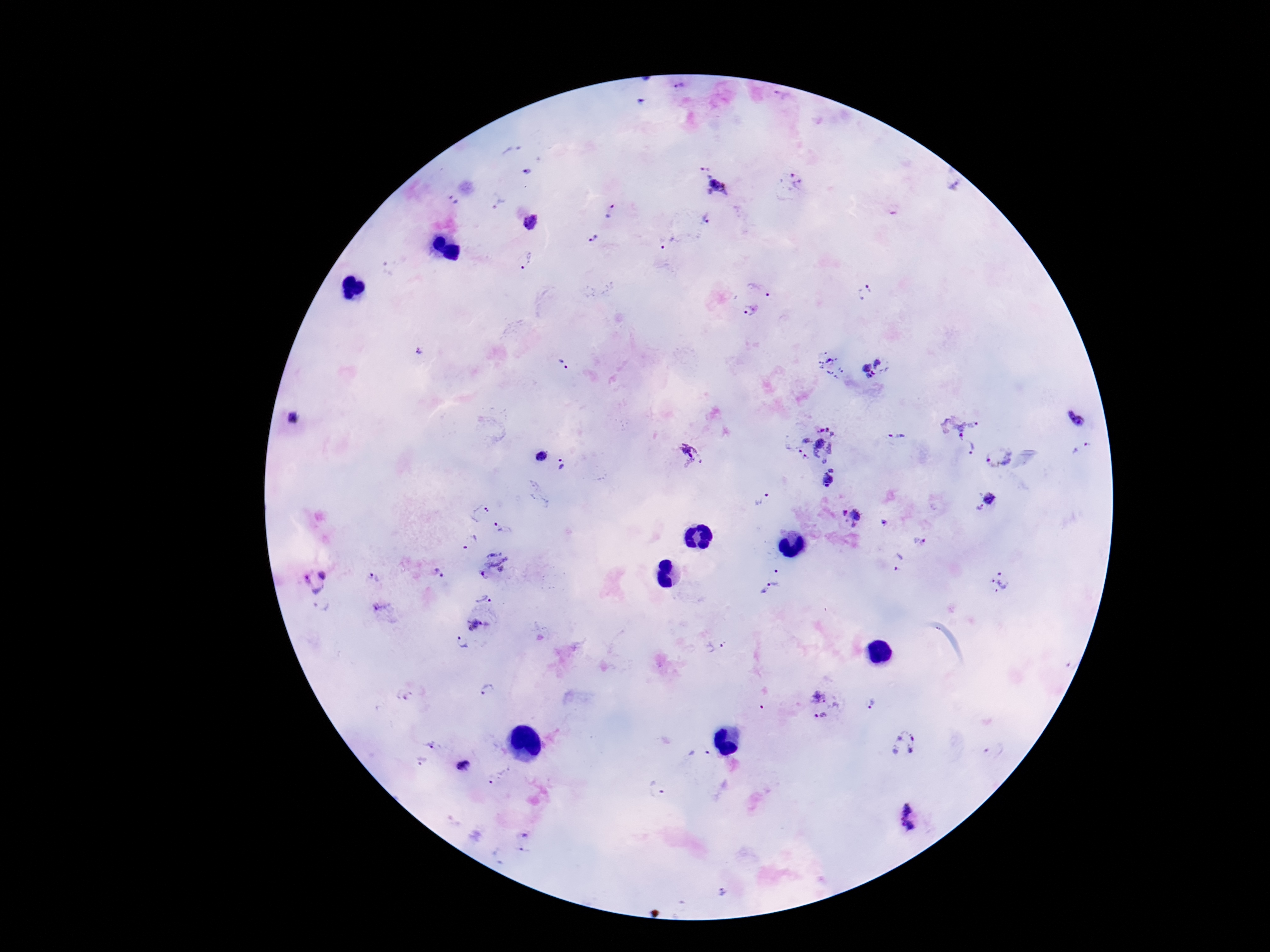

Approximate centers as (x, y) in pixels. Plasmodium parasite locations: (679, 84), (783, 99), (705, 164), (526, 173), (792, 181), (950, 184), (717, 185), (452, 200), (498, 204), (611, 210), (707, 216), (530, 222), (591, 239), (666, 243), (525, 262), (763, 286), (865, 291), (749, 309), (421, 348), (831, 363), (881, 364), (565, 366), (295, 416), (1077, 422), (957, 424), (898, 436), (811, 442), (970, 449), (1084, 452), (690, 454), (539, 455), (998, 456), (563, 467), (832, 468), (827, 481), (990, 496), (760, 500), (976, 509), (478, 512), (853, 517), (885, 523), (502, 527), (468, 541), (920, 541), (898, 562), (493, 566), (438, 573), (777, 576), (374, 578), (314, 581), (1000, 581), (765, 589), (483, 595), (323, 606), (382, 610), (476, 626), (716, 645), (461, 646), (487, 690), (407, 697), (823, 704), (872, 704), (903, 741), (429, 744), (993, 749), (420, 762), (461, 765), (496, 777), (658, 787), (913, 819), (523, 842), (723, 890). Photographed through the microscope eyepiece with a smartphone camera. Single field of view. 100x magnification. Patient malaria status: infected. Giemsa stain. Thick peripheral-blood smear. Image is 1270×952 pixels.